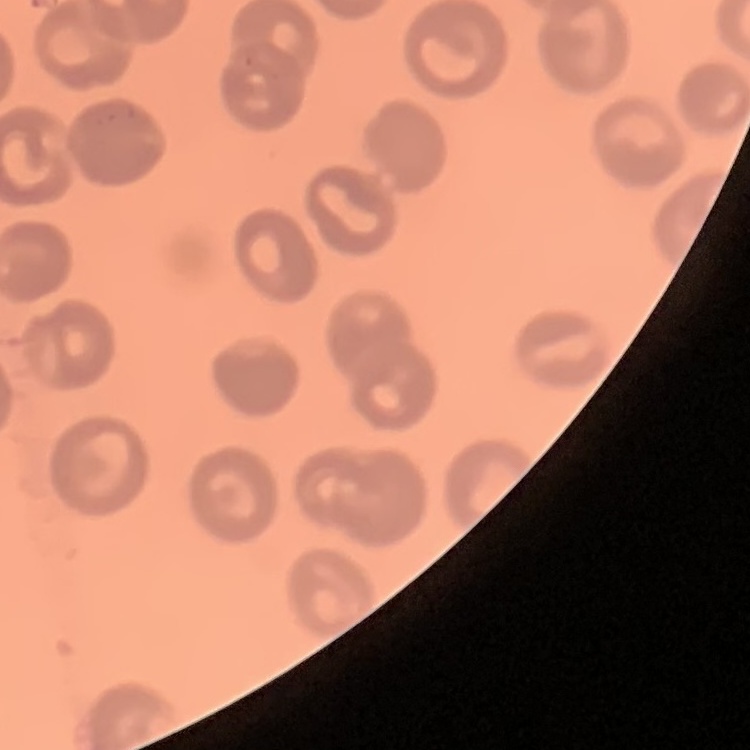 The erythrocytes show no rouleaux formation. Stained with either Field's or Giemsa. Thin blood smear. Square crop of a larger photomicrograph.